Give the position of every Plasmodium parasite visible.
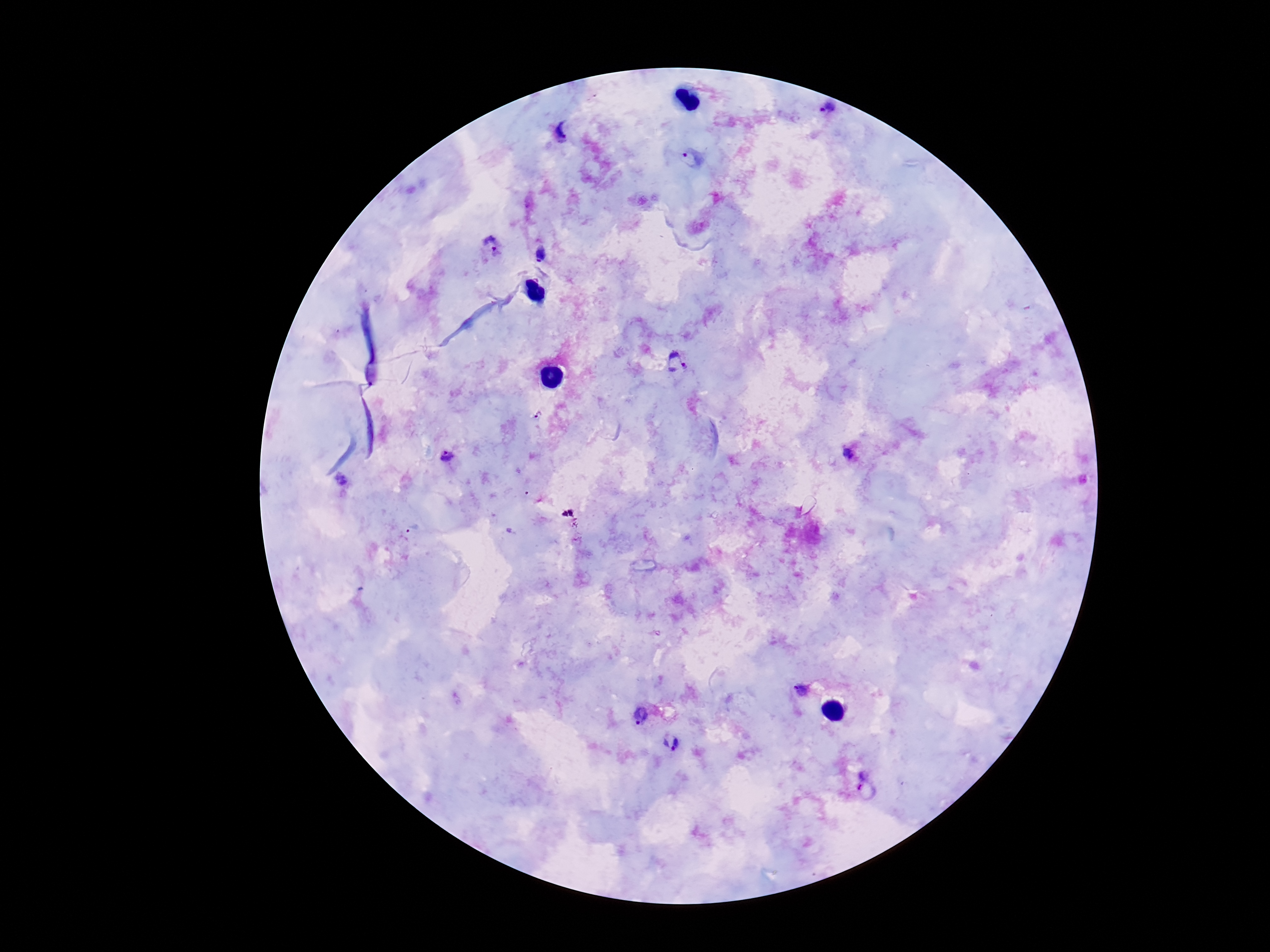

Approximate centers as {x, y} in pixels.
Plasmodium parasites: {826, 112}, {567, 128}, {692, 158}, {493, 245}, {541, 253}, {676, 363}, {537, 416}, {850, 455}, {448, 457}, {340, 479}, {802, 690}, {640, 715}, {670, 743}, {864, 784}.

{
  "patient_malaria_status": "infected",
  "preparation": "thick peripheral-blood smear",
  "image_size": "1270×952 pixels",
  "field_of_view": "one from this slide",
  "magnification": "100x",
  "capture": "smartphone camera through the microscope eyepiece",
  "stain": "Giemsa"
}